Report the malaria status of this cell.
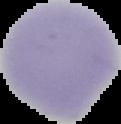

Uninfected.

Summary:
  - Image type: segmented cell region on a black background
  - Image size: 121×124 pixels
  - Preparation: thin blood smear